Locate malaria parasites and leukocytes.
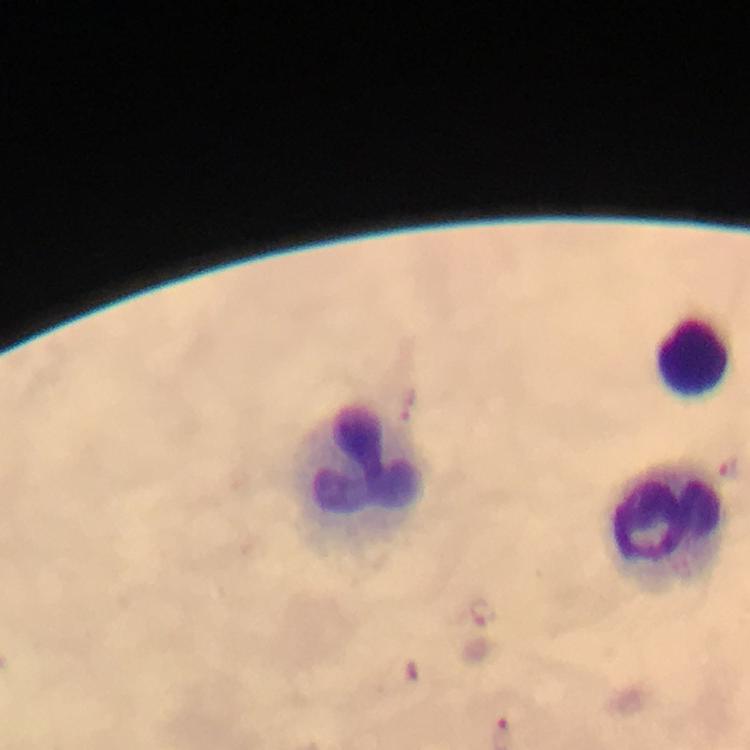
Approximate centers as (x, y) in pixels.
Malaria parasites: (479, 611), (414, 672).
Leukocytes: (696, 356), (358, 472), (667, 526).

Summary:
  - Immersion oil: applied
  - Stain: Giemsa
  - Context: from a diagnostic examination for malaria
  - Image size: 750×750 pixels
  - Preparation: thick blood smear
  - Magnification: 100x
  - Cropped from: one field of view
  - Capture: smartphone camera through the microscope